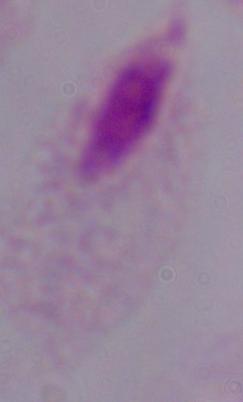

magnification = 1000x
modality = micrograph
identification = trichomonad